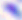
magnification = 400x
modality = photomicrograph
identification = Toxoplasma gondii